Evaluate for Plasmodium parasites.
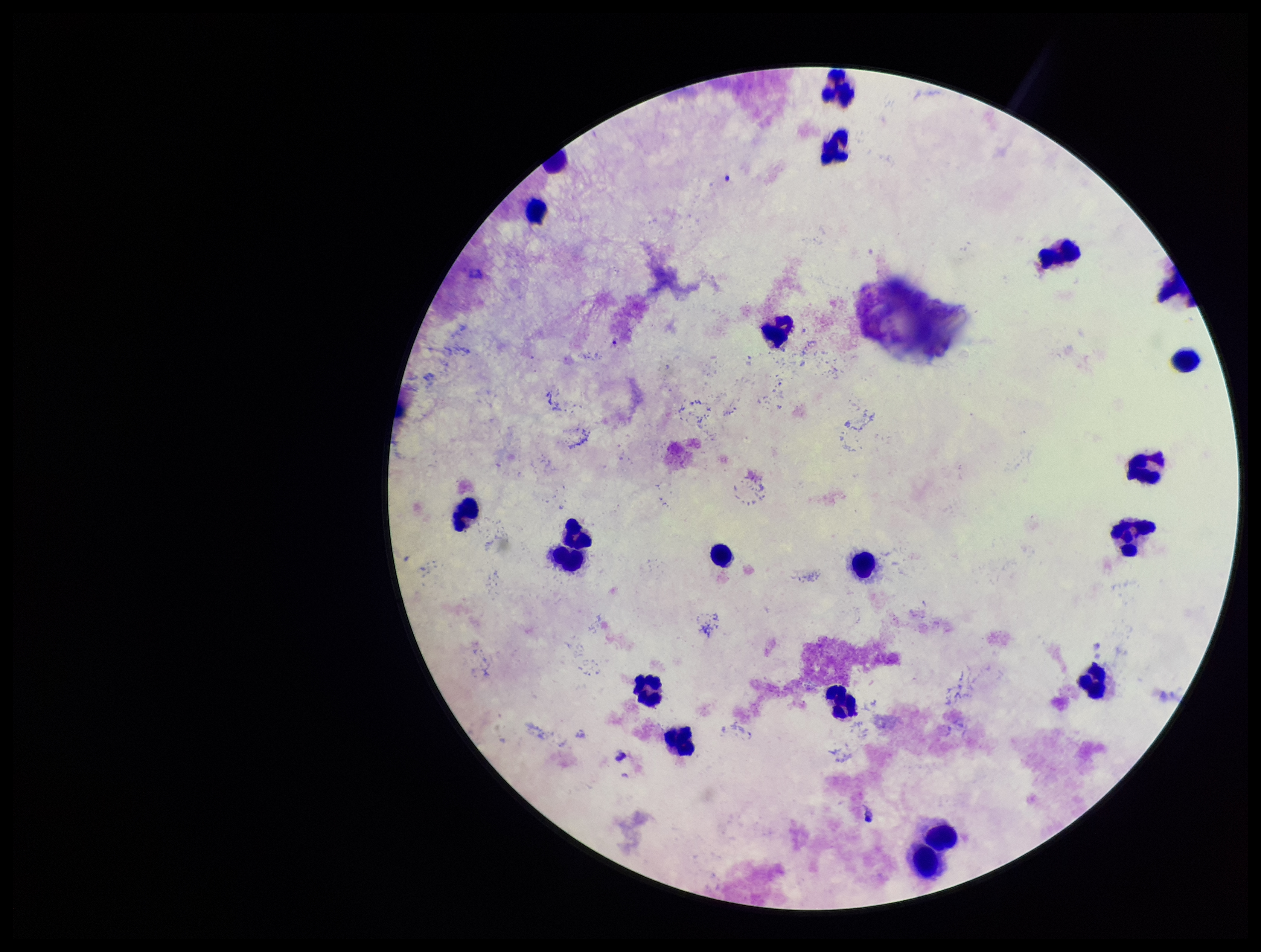
None detected.

Leukocyte count: 22. Parasite count: 0. Image is 1261×952 pixels. Stained with Giemsa. One field from this slide. Photographed through the microscope eyepiece with a smartphone camera. Preparation: thick smear. Patient malaria status: negative.